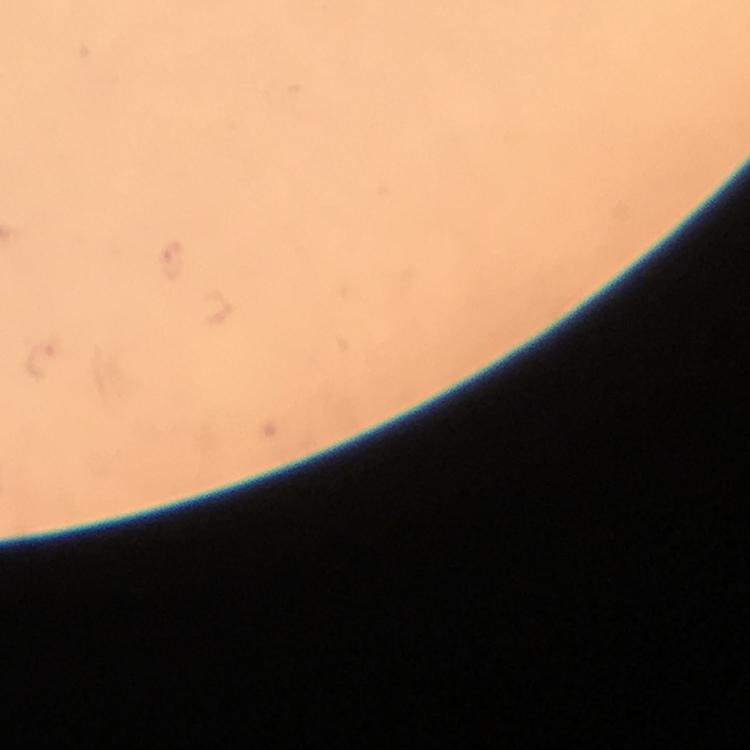 Approximate object centers, in pixels from the top-left corner. Plasmodium parasite locations: (x=42, y=360). Thick blood film. Giemsa-stained preparation. A crop from one field of view. Smartphone photograph taken through a microscope. From a diagnostic examination for malaria. At 100x magnification. Immersion oil was used. Image is 750×750 pixels.